Identify the blood parasite species.
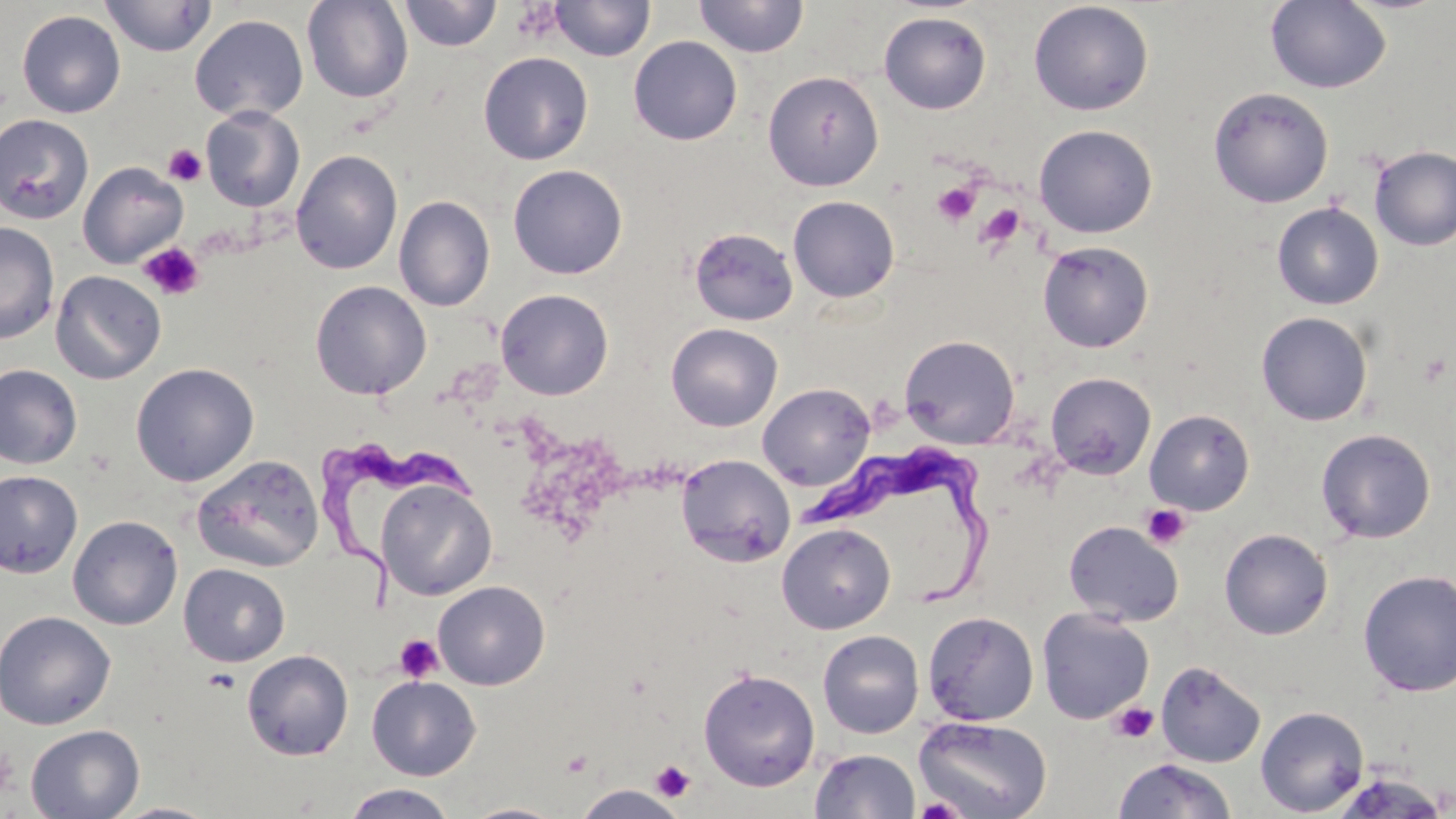
Trypanosoma brucei.

{
  "preparation": "thin blood film",
  "image_size": "1456×819 pixels",
  "trypanosoma_brucei_locations": "approximate bounding boxes as (x1, y1, x2, y2) in pixels: (323, 442, 479, 605), (806, 450, 999, 609)",
  "stain": "May-Grünwald-Giemsa",
  "platelet_locations": "approximate bounding boxes as (x1, y1, x2, y2) in pixels: (510, 3, 563, 43), (162, 144, 207, 186), (931, 180, 981, 226), (977, 203, 1026, 250), (139, 242, 204, 302), (1140, 504, 1191, 550), (394, 634, 444, 683), (1109, 701, 1159, 744), (0, 747, 19, 799), (650, 760, 695, 803), (914, 796, 966, 819)",
  "magnification": "1000x",
  "uninfected_red_blood_cell_locations": "approximate bounding boxes as (x1, y1, x2, y2) in pixels: (99, 0, 216, 57), (302, 0, 413, 103), (694, 0, 809, 58), (1266, 0, 1391, 94), (399, 1, 502, 52), (549, 1, 655, 62), (1028, 1, 1154, 116), (16, 9, 126, 118), (878, 11, 992, 114), (190, 14, 309, 122), (628, 36, 743, 146), (479, 51, 593, 165), (762, 70, 884, 191), (1208, 87, 1333, 208), (200, 106, 305, 212), (0, 114, 94, 224), (1033, 124, 1157, 238), (1370, 145, 1456, 251), (291, 149, 403, 275), (77, 161, 188, 268), (507, 164, 628, 279), (393, 195, 495, 312), (787, 196, 900, 303), (1271, 202, 1384, 310), (0, 222, 59, 344), (689, 228, 798, 326), (1037, 241, 1154, 353), (50, 270, 166, 384), (310, 280, 432, 400), (496, 288, 614, 400), (1256, 311, 1373, 426), (666, 323, 782, 431), (899, 334, 1020, 449), (130, 362, 259, 486), (0, 364, 82, 470), (1045, 372, 1156, 479), (757, 382, 875, 490), (1145, 408, 1255, 515), (1316, 428, 1436, 543), (676, 453, 796, 568), (191, 454, 324, 573), (0, 470, 83, 578), (376, 480, 497, 600), (67, 515, 183, 630), (1063, 520, 1183, 627), (776, 522, 896, 634), (1219, 528, 1333, 640), (178, 563, 291, 667), (1357, 569, 1456, 698), (432, 580, 550, 690), (1037, 607, 1155, 724), (0, 610, 116, 730), (922, 611, 1039, 726), (818, 630, 924, 739), (241, 649, 354, 761), (1155, 661, 1266, 767), (698, 667, 820, 791), (367, 675, 481, 780), (1255, 705, 1370, 816), (913, 715, 1052, 818), (25, 724, 145, 819), (809, 748, 921, 819), (1112, 758, 1237, 818), (340, 784, 459, 819), (569, 784, 690, 818), (108, 802, 223, 819), (459, 802, 570, 819)",
  "modality": "light microscopy",
  "field_of_view": "single"
}